Identify the blood parasite species.
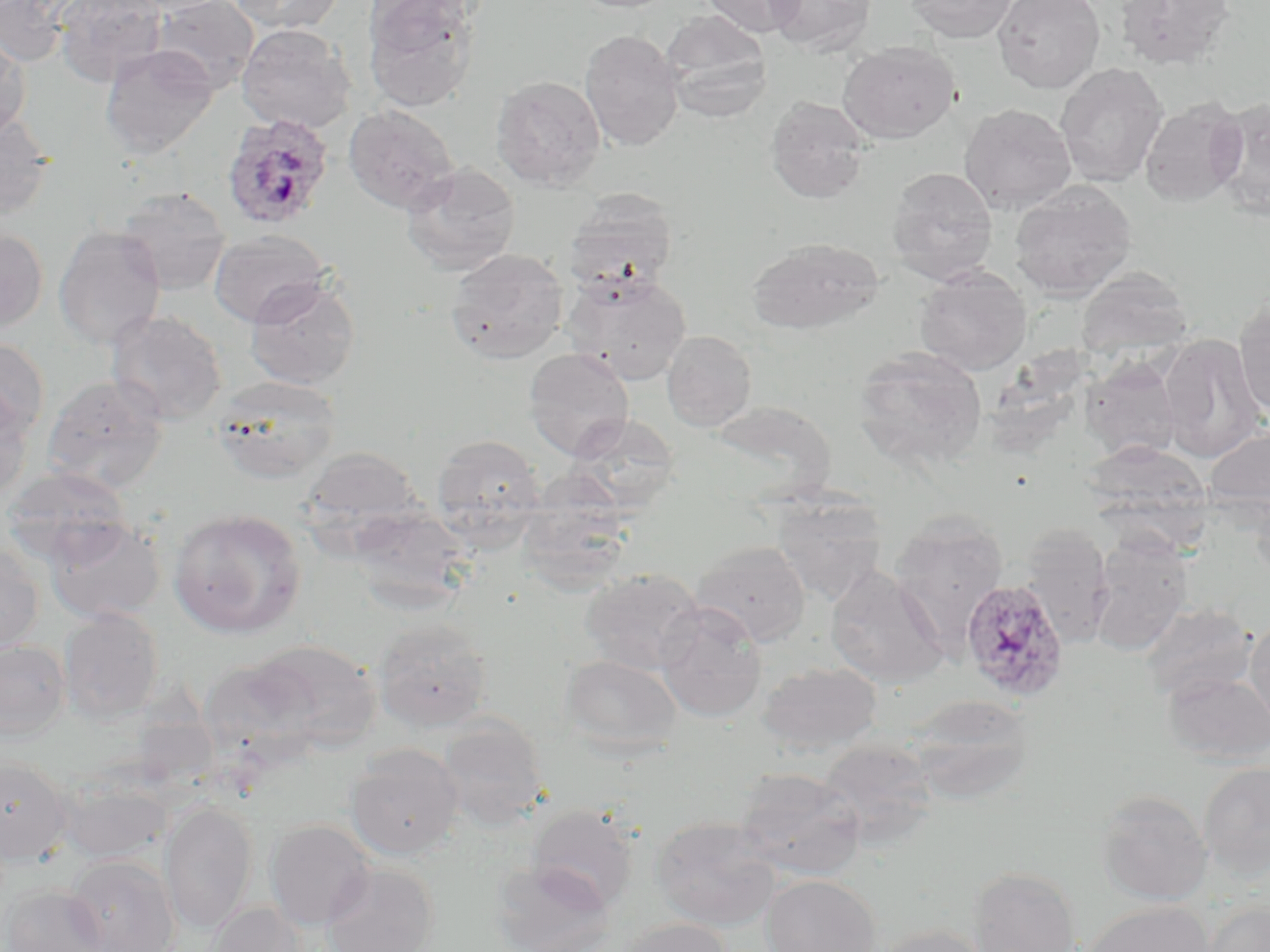

Plasmodium ovale.

Summary:
  - Coordinate format: approximate bounding boxes as [x1, y1, x2, y2] in pixels
  - Uninfected red blood cell locations: [1, 0, 74, 66], [52, 0, 168, 86], [120, 0, 234, 16], [152, 0, 260, 94], [229, 0, 346, 34], [361, 0, 487, 112], [570, 0, 680, 13], [700, 0, 804, 38], [767, 0, 877, 56], [906, 0, 1018, 43], [993, 0, 1105, 93], [1114, 0, 1236, 71], [660, 11, 773, 120], [236, 24, 356, 134], [1, 30, 31, 138], [579, 30, 684, 152], [838, 40, 961, 144], [100, 44, 218, 158], [1055, 62, 1168, 188], [490, 75, 606, 190], [765, 96, 871, 203], [1208, 97, 1270, 218], [1139, 98, 1248, 206], [959, 103, 1077, 214], [342, 104, 460, 214], [0, 112, 55, 220], [401, 163, 521, 275], [886, 167, 998, 285], [1009, 181, 1136, 300], [115, 186, 231, 295], [564, 190, 679, 293], [53, 225, 166, 350], [0, 227, 48, 333], [207, 229, 332, 327], [747, 237, 884, 334], [445, 248, 569, 365], [1076, 265, 1194, 356], [913, 267, 1033, 375], [562, 270, 692, 385], [244, 277, 361, 391], [1233, 297, 1270, 419], [106, 309, 228, 425], [662, 330, 757, 431], [1159, 335, 1269, 460], [0, 336, 49, 442], [851, 346, 989, 470], [524, 348, 634, 460], [1080, 358, 1182, 462], [42, 375, 168, 494], [210, 376, 343, 483], [0, 383, 33, 505], [707, 400, 836, 503], [567, 413, 681, 513], [1203, 420, 1270, 519], [430, 433, 545, 540], [1079, 442, 1214, 530], [299, 447, 425, 543], [0, 467, 133, 567], [1248, 490, 1270, 589], [771, 496, 887, 606], [346, 506, 475, 613], [168, 508, 306, 638], [888, 512, 1008, 650], [45, 517, 165, 623], [1019, 523, 1115, 649], [1088, 536, 1193, 655], [691, 540, 810, 646], [0, 543, 44, 655], [825, 566, 949, 688], [580, 567, 706, 675], [654, 602, 768, 724], [1140, 602, 1257, 703], [59, 607, 164, 723], [1245, 613, 1270, 734], [372, 617, 494, 733], [251, 639, 382, 751], [0, 640, 70, 741], [560, 654, 683, 758], [197, 657, 321, 765], [757, 661, 882, 755], [1162, 670, 1270, 765], [905, 694, 1034, 804], [437, 716, 548, 830], [816, 737, 939, 849], [344, 744, 464, 860], [0, 757, 73, 864], [1199, 762, 1270, 877], [732, 767, 866, 880], [56, 777, 172, 864], [1095, 789, 1212, 906], [160, 801, 258, 934], [526, 804, 639, 914], [651, 816, 782, 931], [265, 819, 376, 930], [65, 854, 180, 952], [489, 859, 615, 952], [321, 862, 439, 952], [968, 866, 1081, 952], [761, 874, 880, 952], [1, 883, 107, 951], [1203, 899, 1269, 952], [1082, 900, 1214, 952], [208, 902, 310, 952], [614, 917, 733, 952], [869, 924, 994, 952]
  - Plasmodium ovale-infected red blood cell locations: [221, 112, 335, 230], [961, 578, 1069, 700]
  - Magnification: 1000x
  - Preparation: thin blood film
  - Field of view: one of a larger specimen
  - Modality: optical microscopy
  - Stain: May-Grünwald-Giemsa
  - Image size: 1270×952 pixels